Locate platelets.
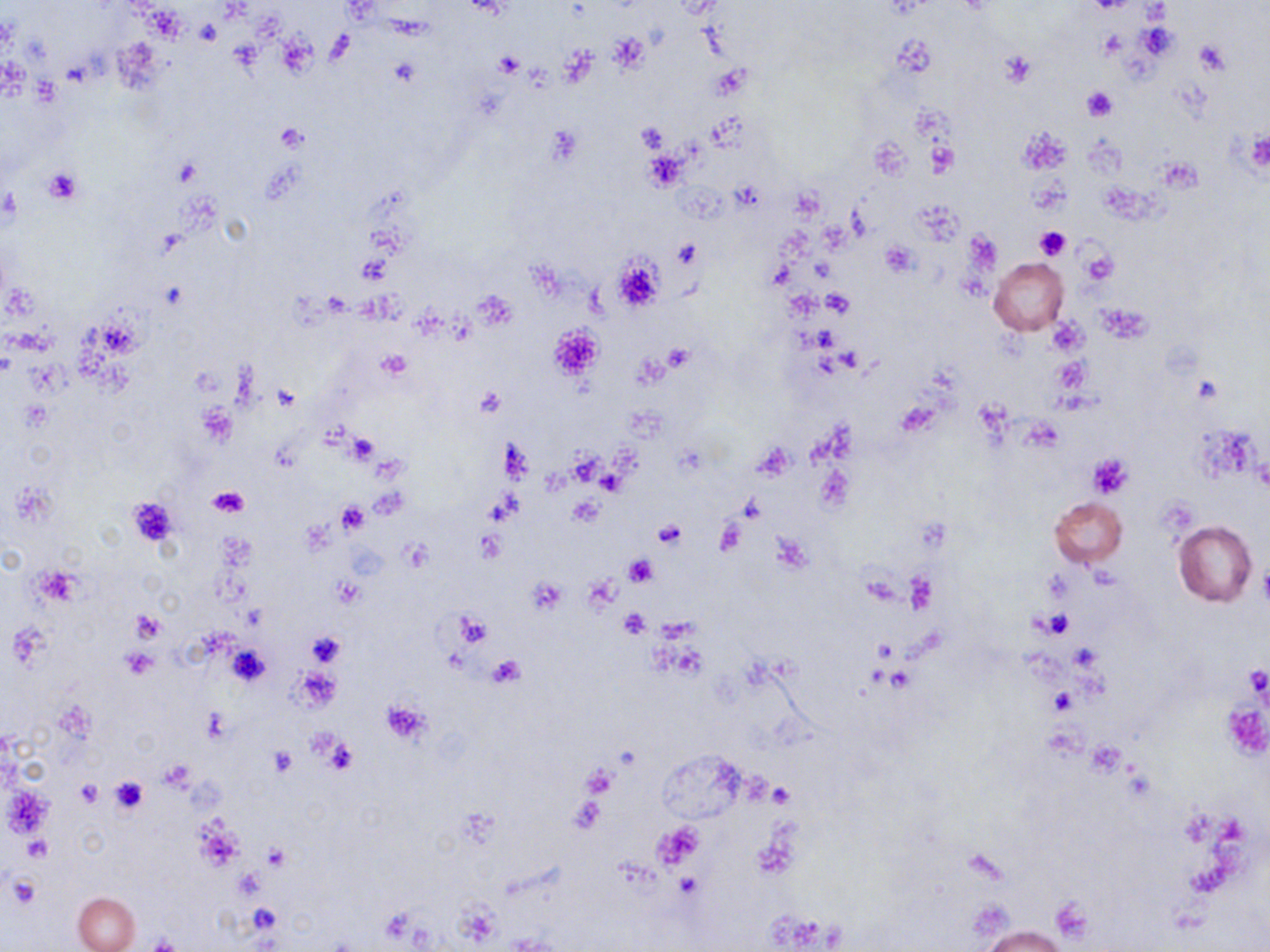
Approximate bounding boxes as (x1, y1, x2, y2) in pixels.
Platelets: (195, 20, 221, 45), (608, 34, 648, 72), (277, 35, 316, 75), (1194, 40, 1230, 74), (1000, 52, 1036, 86), (495, 53, 525, 78), (1081, 87, 1118, 121), (635, 122, 672, 153), (275, 124, 306, 151), (1244, 131, 1270, 175), (926, 138, 959, 177), (642, 149, 686, 190), (43, 169, 82, 203), (1029, 177, 1069, 215), (1034, 225, 1071, 260), (674, 240, 699, 267), (881, 240, 917, 279), (1082, 249, 1116, 285), (614, 256, 664, 309), (821, 291, 855, 317), (1101, 306, 1149, 341), (548, 323, 605, 382), (664, 344, 692, 371), (374, 350, 413, 383), (1053, 358, 1089, 393), (474, 386, 505, 416), (348, 432, 379, 462), (1086, 452, 1132, 498), (208, 487, 248, 517), (127, 495, 182, 550), (567, 497, 602, 526), (337, 503, 367, 534), (653, 521, 684, 549), (475, 529, 505, 563), (401, 542, 430, 572), (625, 555, 655, 587), (1259, 560, 1270, 609), (36, 567, 79, 607), (526, 577, 567, 616), (334, 579, 364, 607), (619, 608, 651, 636), (1040, 609, 1076, 638), (130, 610, 165, 641), (454, 613, 492, 646), (306, 630, 344, 668), (228, 642, 270, 686), (120, 650, 159, 678), (488, 655, 525, 686), (1244, 667, 1268, 701), (380, 700, 432, 745), (1222, 702, 1270, 761), (201, 709, 231, 742), (315, 736, 357, 775), (270, 747, 296, 774), (160, 761, 194, 792), (581, 764, 617, 799), (109, 777, 147, 815), (77, 780, 104, 807), (768, 783, 794, 809), (3, 785, 51, 839), (24, 837, 52, 861), (264, 845, 289, 870), (676, 873, 700, 900), (5, 876, 40, 910), (1051, 899, 1093, 943), (249, 904, 280, 932).

slide-level diagnosis = negative for blood parasites
magnification = 1000x
uninfected red blood cell locations = approximate bounding boxes as (x1, y1, x2, y2) in pixels: (989, 258, 1068, 335), (1050, 497, 1127, 567), (1173, 520, 1256, 607), (74, 892, 139, 952), (974, 923, 1071, 951)
modality = light microscopy
field of view = single
image size = 1270×952 pixels
stain = May-Grünwald-Giemsa
preparation = thin blood smear